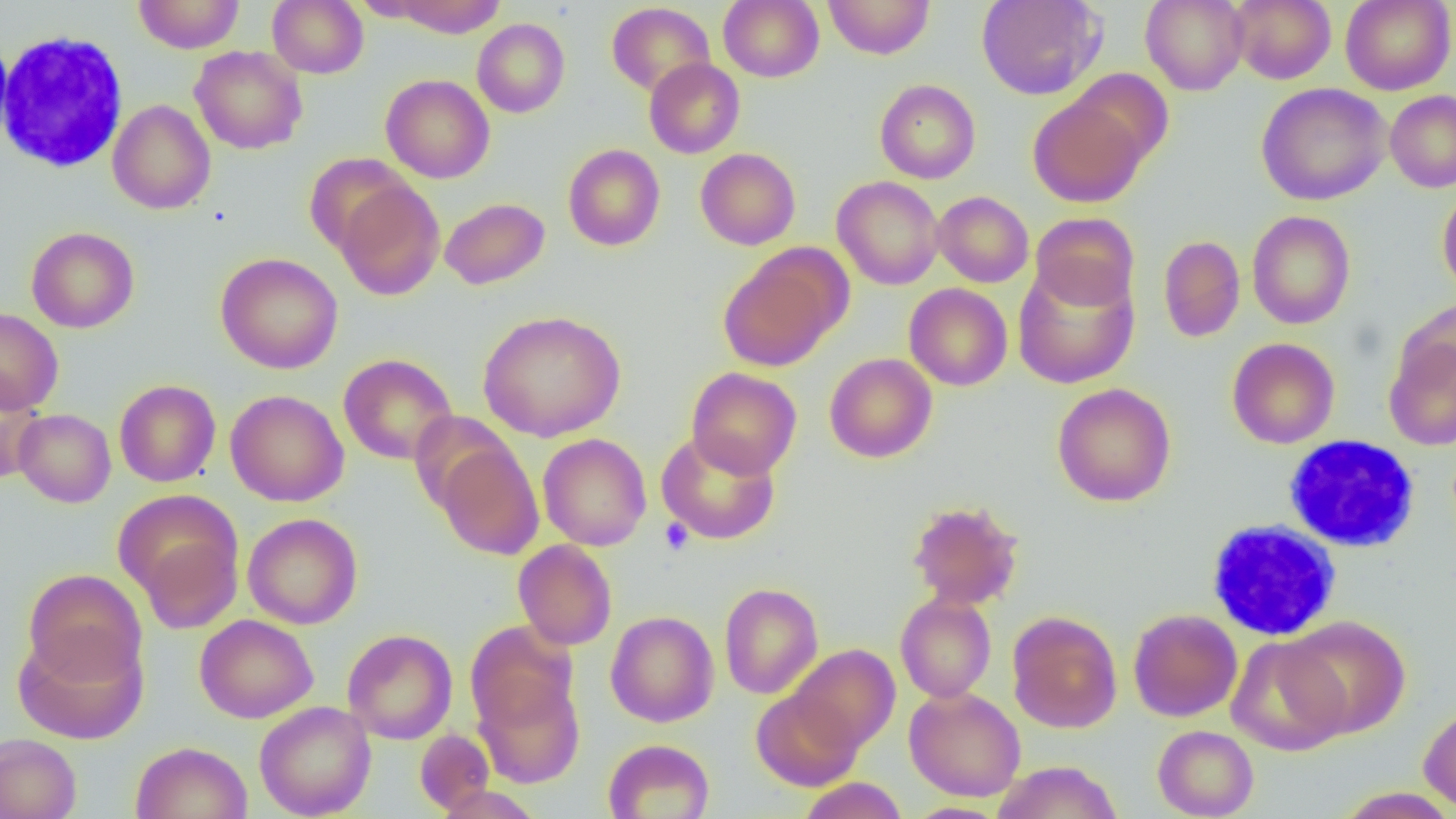

Summary:
  - Coordinate format: approximate bounding boxes as (x1, y1, x2, y2) in pixels
  - White blood cell locations: (0, 31, 128, 173), (1284, 435, 1420, 552), (1206, 519, 1342, 641)
  - Uninfected red blood cell locations: (133, 0, 245, 54), (267, 0, 369, 78), (387, 0, 508, 37), (719, 0, 824, 82), (823, 0, 935, 59), (976, 0, 1105, 100), (1140, 0, 1248, 95), (1229, 0, 1336, 84), (1340, 0, 1455, 95), (606, 3, 715, 97), (472, 18, 570, 118), (0, 35, 14, 151), (190, 46, 307, 154), (644, 58, 745, 159), (1067, 69, 1174, 168), (381, 74, 495, 183), (875, 79, 981, 184), (1256, 83, 1391, 206), (1385, 90, 1456, 192), (1029, 95, 1147, 208), (108, 100, 216, 214), (563, 144, 665, 251), (695, 148, 801, 249), (304, 153, 413, 256), (832, 176, 944, 290), (334, 179, 445, 301), (1437, 186, 1456, 300), (933, 191, 1033, 287), (439, 197, 550, 290), (1246, 210, 1356, 329), (1030, 212, 1139, 311), (26, 226, 140, 333), (1158, 235, 1245, 343), (216, 252, 343, 374), (718, 252, 843, 372), (1013, 261, 1139, 388), (904, 283, 1012, 391), (1396, 298, 1456, 396), (0, 308, 63, 414), (478, 310, 626, 442), (1383, 336, 1456, 450), (1226, 337, 1340, 449), (338, 353, 458, 465), (824, 353, 937, 463), (686, 367, 801, 478), (0, 375, 44, 484), (114, 379, 221, 487), (1052, 383, 1176, 507), (225, 390, 349, 506), (13, 408, 116, 507), (656, 430, 781, 545), (537, 433, 652, 550), (434, 439, 544, 560), (114, 489, 244, 624), (907, 500, 1024, 610), (243, 513, 363, 629), (513, 540, 617, 650), (22, 568, 147, 688), (719, 582, 823, 699), (895, 592, 997, 703), (1128, 608, 1242, 722), (605, 611, 719, 727), (1007, 611, 1122, 734), (194, 614, 318, 723), (1283, 615, 1411, 738), (465, 620, 579, 733), (13, 626, 149, 745), (342, 628, 458, 744), (1227, 636, 1349, 756), (788, 644, 900, 754), (474, 676, 585, 788), (904, 686, 1026, 801), (751, 688, 863, 791), (254, 701, 376, 818), (1418, 703, 1456, 813), (1152, 725, 1259, 819), (414, 729, 495, 814), (0, 733, 82, 819), (603, 738, 714, 819), (130, 741, 252, 819), (991, 760, 1123, 819), (797, 777, 909, 819), (1336, 787, 1456, 819), (904, 802, 1009, 819)
  - Platelet locations: (659, 517, 694, 555)
  - Slide-level diagnosis: negative for blood parasites
  - Magnification: 1000x
  - Field of view: single
  - Preparation: thin blood film
  - Modality: light microscopy
  - Image size: 1456×819 pixels